Give the position of every Plasmodium parasite visible.
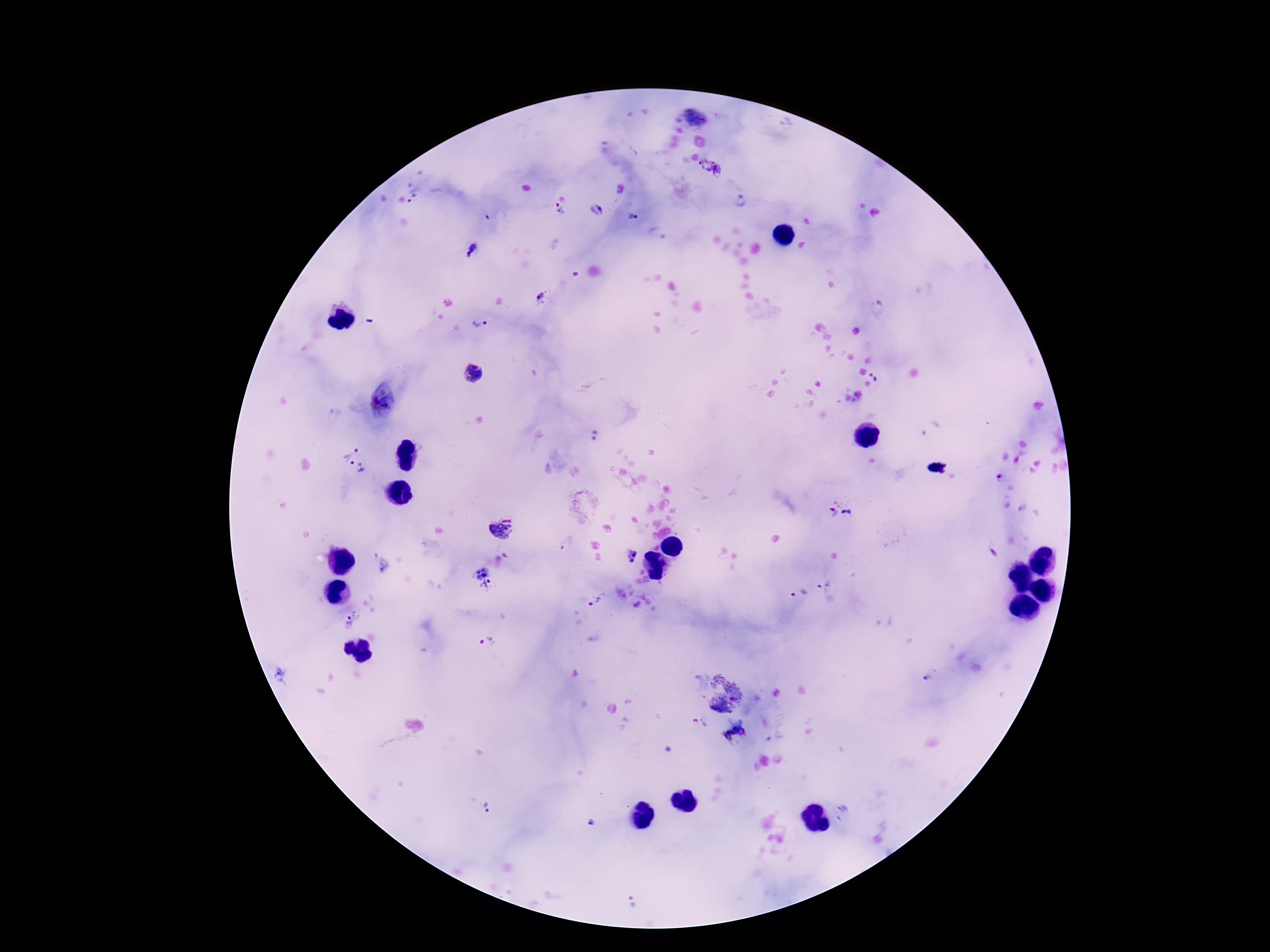
Approximate centers as {x, y} in pixels.
Plasmodium parasites: {696, 116}, {714, 170}, {413, 199}, {740, 201}, {557, 210}, {633, 216}, {472, 251}, {542, 298}, {480, 323}, {472, 373}, {877, 376}, {382, 401}, {596, 436}, {356, 461}, {842, 509}, {501, 529}, {632, 557}, {384, 565}, {483, 578}, {825, 584}, {797, 595}, {594, 603}, {355, 619}, {489, 644}, {932, 675}, {279, 677}, {721, 695}, {486, 809}, {589, 821}, {631, 903}.

patient_malaria_status: infected
stain: Giemsa
field_of_view: one from this slide
magnification: 100x
preparation: thick blood smear
image_size: 1270×952 pixels
capture: smartphone camera through the microscope eyepiece